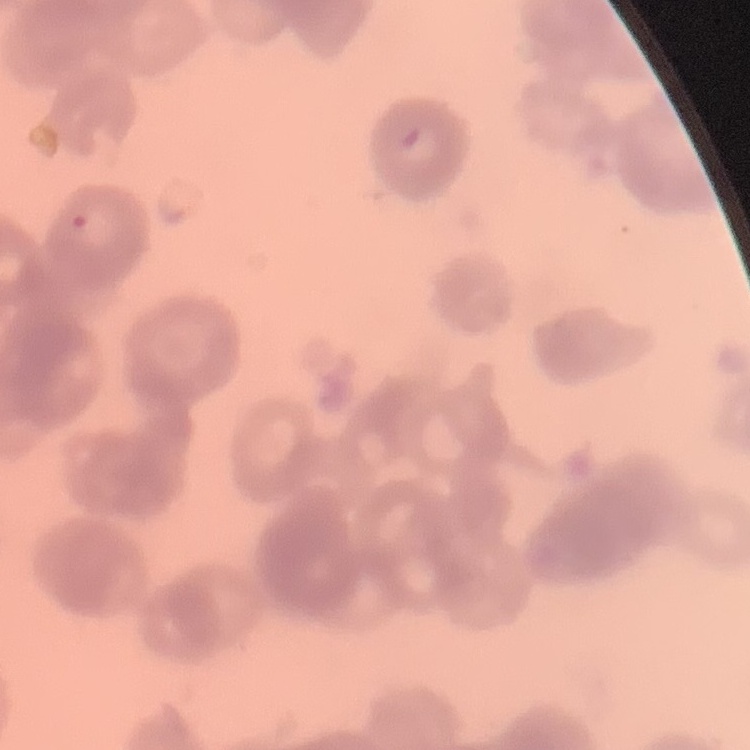 The red blood cells exhibit rouleaux formation. Thin blood film. One tile cut from a larger photomicrograph. Field's or Giemsa stain.